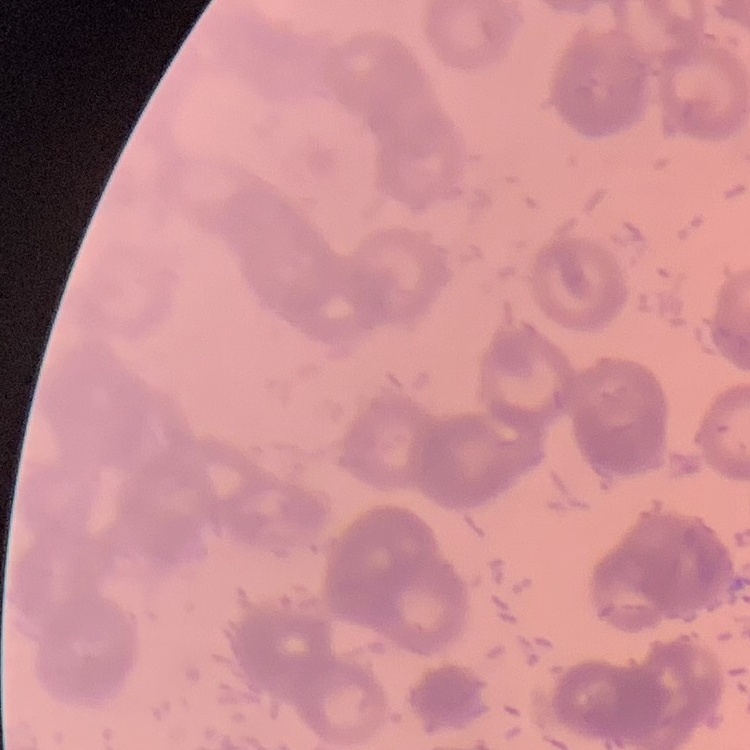
Summary:
  - Red blood cell morphology: rouleaux formation
  - Image type: square crop of a larger photomicrograph
  - Stain: Field's or Giemsa
  - Preparation: thin blood smear